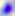 Captured at 400x magnification. Toxoplasma gondii is seen. Photomicrograph.